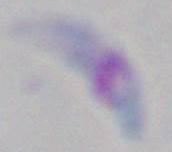
Micrograph. 1000x magnification. Toxoplasma gondii is seen.